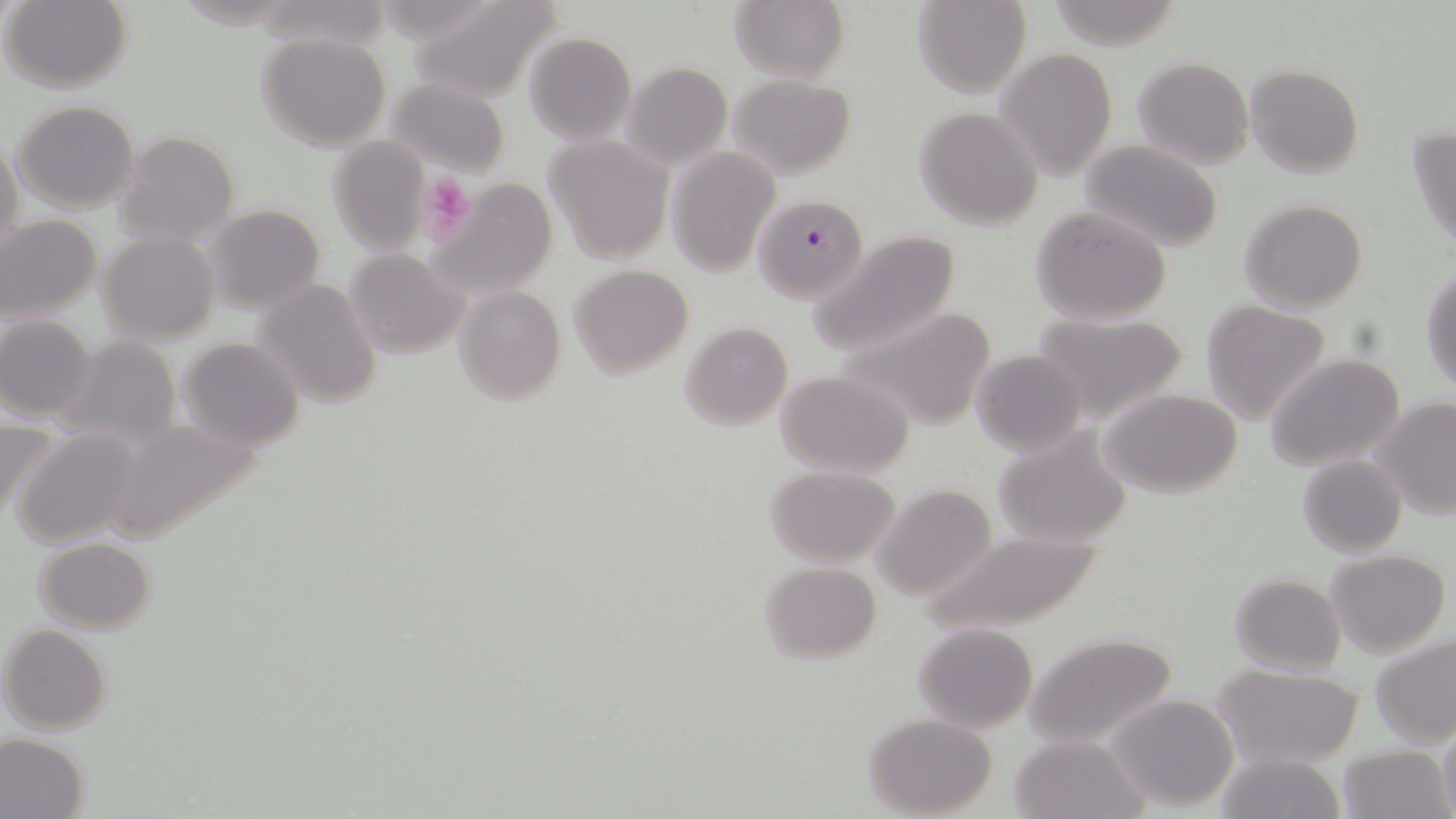 Approximate bounding boxes as [x1, y1, x2, y2] in pixels. Platelet locations: [418, 173, 476, 244]. Uninfected red blood cell locations: [4, 0, 131, 93], [409, 0, 564, 105], [912, 0, 1031, 98], [729, 1, 848, 83], [256, 30, 393, 152], [524, 32, 636, 146], [995, 48, 1117, 179], [1132, 56, 1254, 169], [620, 62, 732, 171], [1245, 64, 1365, 179], [727, 74, 855, 178], [387, 78, 512, 177], [13, 100, 142, 213], [912, 107, 1044, 230], [1407, 127, 1456, 250], [111, 130, 240, 247], [545, 135, 675, 265], [328, 137, 431, 253], [1078, 138, 1225, 251], [0, 139, 24, 266], [664, 147, 780, 279], [428, 176, 557, 299], [1239, 199, 1368, 315], [201, 205, 325, 313], [1029, 205, 1175, 327], [0, 214, 103, 325], [810, 225, 963, 354], [98, 231, 220, 345], [342, 247, 469, 357], [568, 264, 694, 380], [1421, 266, 1455, 398], [251, 279, 383, 408], [453, 285, 565, 405], [1200, 301, 1332, 424], [835, 306, 1001, 433], [1030, 313, 1192, 424], [0, 315, 98, 422], [680, 322, 794, 431], [177, 336, 304, 450], [59, 337, 182, 446], [971, 349, 1088, 456], [1265, 354, 1407, 471], [774, 369, 917, 480], [1099, 388, 1246, 497], [1374, 397, 1456, 519], [0, 416, 59, 523], [106, 420, 276, 559], [992, 426, 1134, 548], [10, 427, 145, 549], [1298, 454, 1405, 557], [763, 464, 901, 567], [873, 484, 997, 600], [915, 529, 1110, 636], [35, 537, 156, 632], [1325, 549, 1450, 658], [759, 559, 881, 662], [1228, 572, 1346, 675], [1, 623, 113, 735], [913, 623, 1037, 732], [1026, 633, 1178, 749], [1369, 633, 1456, 747], [1215, 666, 1363, 767], [1103, 691, 1242, 811], [864, 714, 997, 818], [1438, 715, 1456, 819], [0, 732, 89, 819], [1010, 733, 1146, 818], [1337, 744, 1453, 819], [1214, 750, 1346, 819]. Plasmodium falciparum-infected red blood cell locations: [753, 194, 869, 305]. Slide-level diagnosis: Plasmodium falciparum. Image is 1456×819 pixels. Optical microscopy. Thin blood film. 1000x magnification. May-Grünwald-Giemsa stain. Single field of view.